Outline platelets.
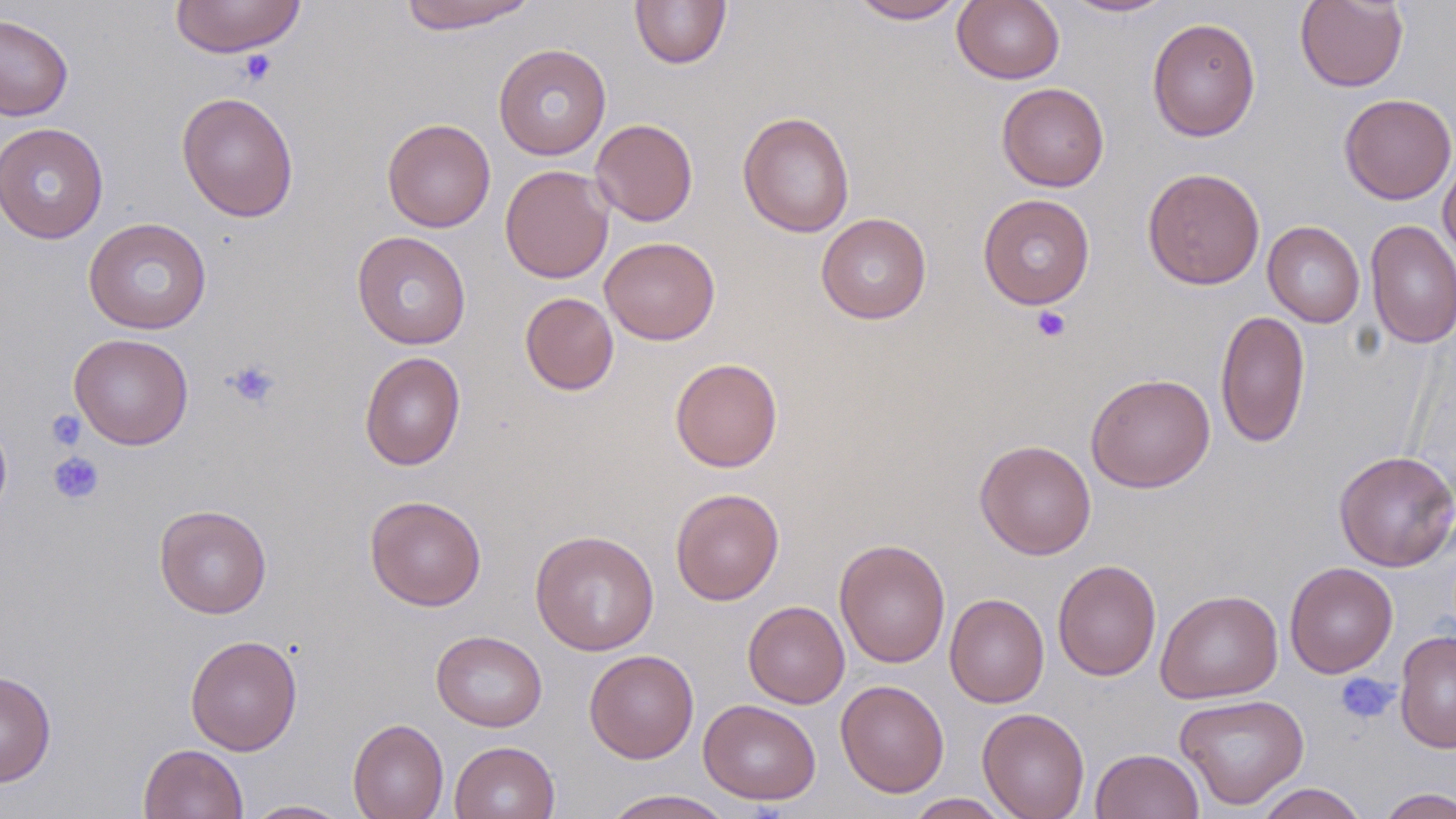

Approximate bounding boxes as (x1, y1, x2, y2) in pixels.
Platelets: (238, 49, 277, 86), (1031, 305, 1072, 342), (224, 358, 282, 410), (47, 409, 86, 450), (47, 452, 104, 505), (1335, 673, 1397, 724).

slide_level_diagnosis: no evidence of blood parasites
uninfected_red_blood_cell_locations: 'approximate bounding boxes as (x1, y1, x2, y2) in pixels: (169, 0, 306, 58), (395, 0, 538, 33), (630, 0, 732, 69), (848, 0, 967, 24), (953, 0, 1065, 84), (1059, 0, 1177, 18), (1295, 0, 1408, 92), (0, 13, 74, 121), (1147, 17, 1261, 142), (494, 43, 611, 160), (997, 83, 1109, 191), (176, 91, 299, 222), (1339, 93, 1456, 205), (737, 111, 855, 238), (382, 118, 496, 232), (590, 118, 698, 226), (0, 122, 109, 244), (1438, 155, 1456, 265), (500, 164, 614, 283), (1142, 167, 1265, 290), (977, 193, 1095, 310), (815, 213, 932, 324), (83, 217, 212, 334), (1365, 219, 1456, 350), (1263, 221, 1365, 327), (352, 231, 471, 349), (600, 236, 720, 345), (520, 292, 619, 395), (1215, 309, 1310, 448), (69, 333, 194, 450), (359, 351, 466, 470), (670, 357, 783, 472), (1086, 373, 1215, 493), (0, 412, 12, 524), (975, 439, 1096, 559), (1334, 450, 1456, 572), (670, 488, 785, 605), (365, 495, 487, 611), (154, 504, 272, 619), (530, 530, 659, 655), (834, 539, 951, 668), (1053, 560, 1161, 680), (1285, 561, 1398, 678), (1155, 589, 1283, 704), (944, 593, 1048, 708), (743, 601, 849, 708), (431, 630, 547, 731), (1394, 630, 1456, 753), (185, 634, 303, 756), (584, 649, 699, 763), (0, 670, 56, 786), (836, 679, 950, 797), (1175, 692, 1310, 810), (698, 698, 821, 805), (977, 707, 1090, 819), (348, 718, 448, 819), (450, 741, 560, 819), (139, 743, 248, 819), (1090, 748, 1205, 819), (1255, 783, 1368, 819), (1377, 787, 1456, 818), (600, 789, 737, 818), (904, 793, 1015, 818), (243, 800, 351, 818)'
image_size: 1456×819 pixels
modality: light microscopy
field_of_view: single
preparation: thin blood smear
magnification: 1000x
stain: May-Grünwald-Giemsa